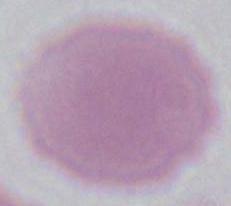

Micrograph. Captured at 1000x magnification. An erythrocyte is shown.